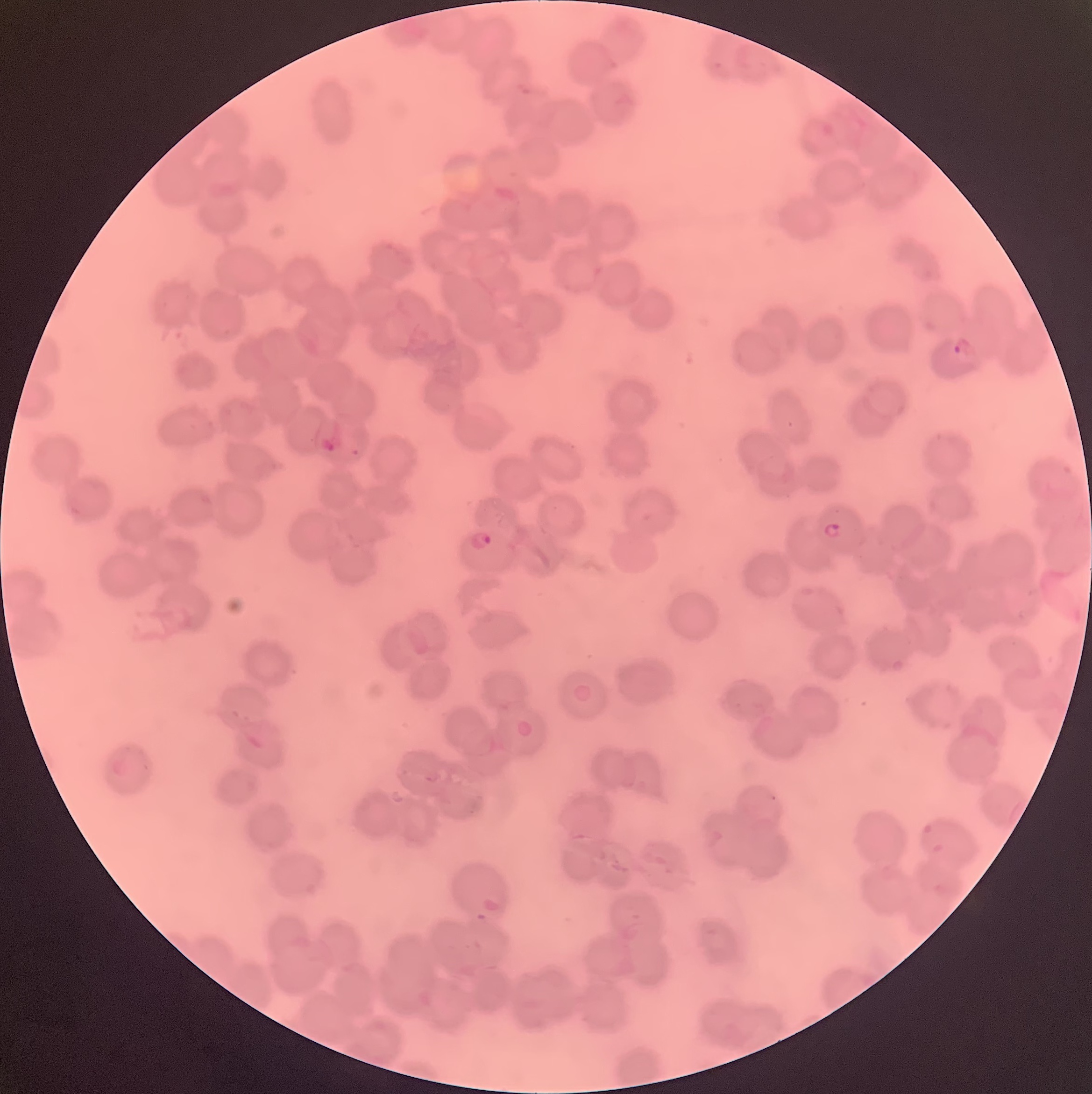

{
  "preparation": "thin blood film",
  "modality": "light microscopy",
  "image_size": "1092×1094 pixels",
  "plasmodium_parasite_locations": "approximate bounding boxes as (x1,y1)-(x2,y2) corner pairs in pixels: (952,336)-(977,360), (320,434)-(342,452), (819,522)-(842,540), (469,530)-(492,551)",
  "red_blood_cell_morphology": "rouleaux formation"
}